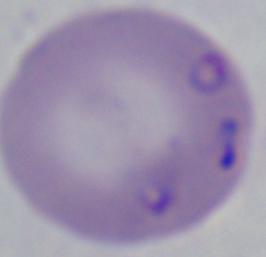
Micrograph. 1000x magnification. A Babesia parasite is shown.